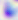

{
  "identification": "Toxoplasma gondii",
  "modality": "micrograph",
  "magnification": "400x"
}